Name the parasite shown.
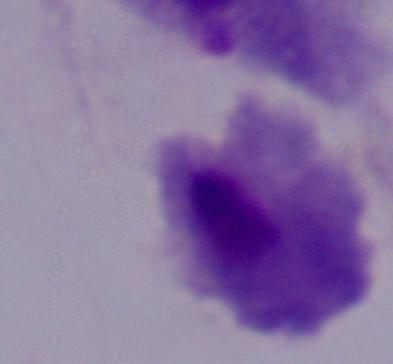

A trichomonad.

magnification = 1000x
modality = photomicrograph